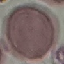

result = negative for malaria parasites
capture = smartphone camera at the microscope eyepiece
preparation = thin blood film
stain = Giemsa
image type = automatically extracted cell patch, resized to 64 × 64 pixels